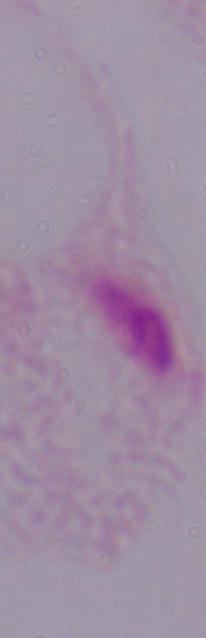

Summary:
  - Modality: micrograph
  - Identification: trichomonad
  - Magnification: 1000x